Report the malaria status of this cell.
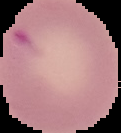

It is parasitized.

Summary:
  - Preparation: thin blood smear
  - Image type: segmented cell region with the area outside set to black
  - Image size: 121×133 pixels